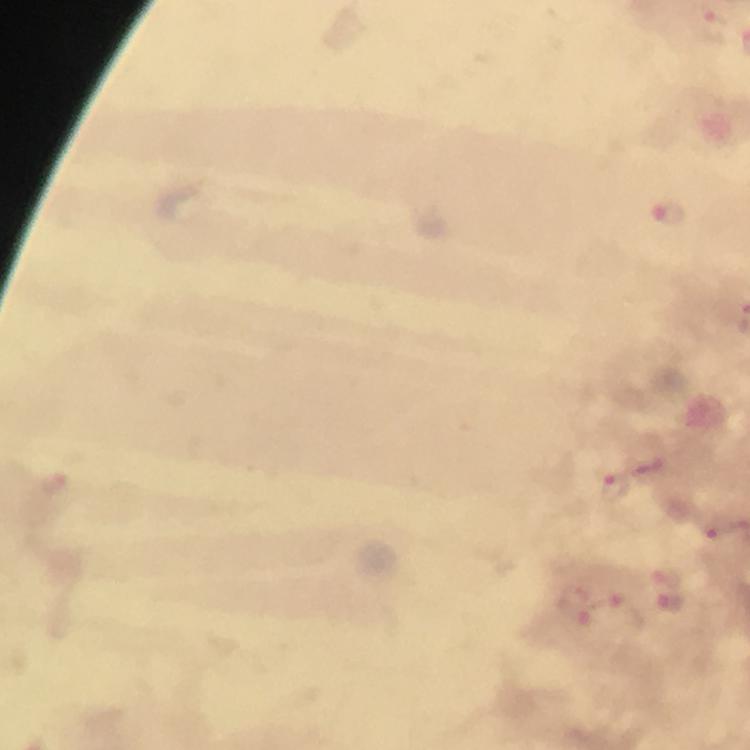
{
  "stain": "Giemsa",
  "capture": "smartphone camera through the microscope",
  "plasmodium_parasite_locations": "approximate object centers, in pixels from the top-left corner: (x=711, y=21), (x=667, y=215), (x=615, y=489), (x=667, y=575), (x=672, y=603), (x=575, y=604), (x=621, y=613)",
  "magnification": "100x",
  "image_size": "750×750 pixels",
  "cropped_from": "a single field of view",
  "immersion_oil": "applied",
  "preparation": "thick blood film",
  "context": "from a diagnostic examination for malaria"
}